Give the position of every malaria parasite.
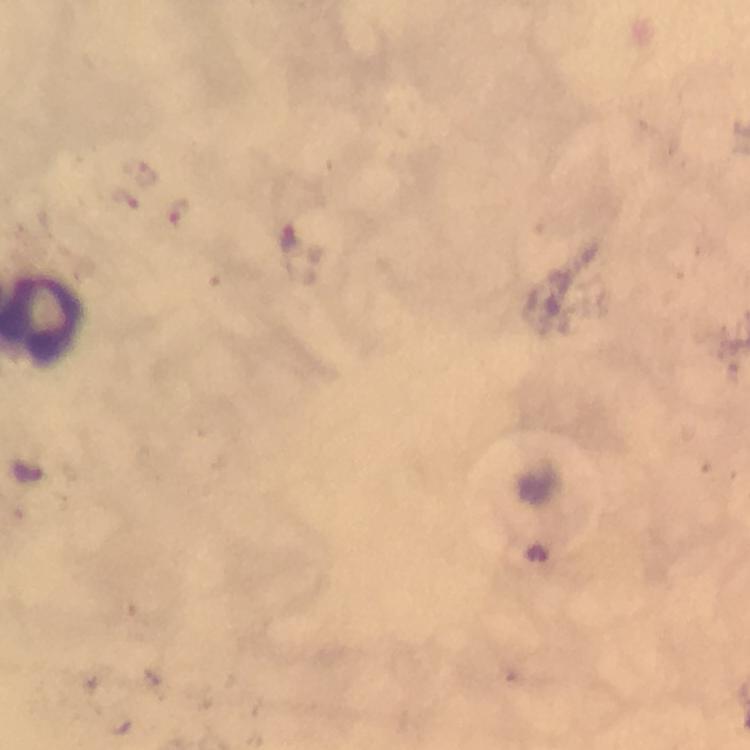

Approximate centers as (x, y) in pixels.
Malaria parasites: (147, 172), (130, 201), (179, 214).

Summary:
  - Preparation: thick blood smear
  - Stain: Giemsa
  - Cropped from: one field of view
  - Magnification: 100x
  - Capture: smartphone photograph through a microscope
  - Image size: 750×750 pixels
  - Context: from a diagnostic examination for malaria
  - Immersion oil: used